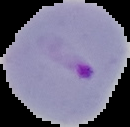 Segmented cell region on a black background. Image is 130×127 pixels. From a thin blood smear. Malaria status: parasitized.